State which parasite is depicted.
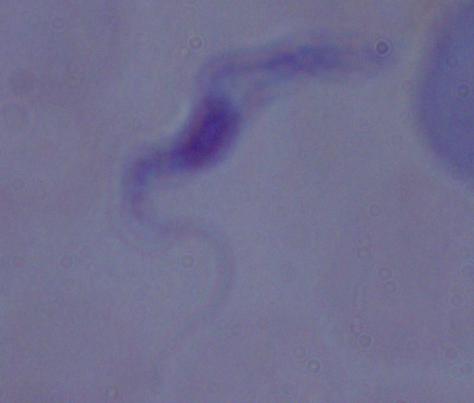

A trypanosome.

magnification = 1000x
modality = micrograph